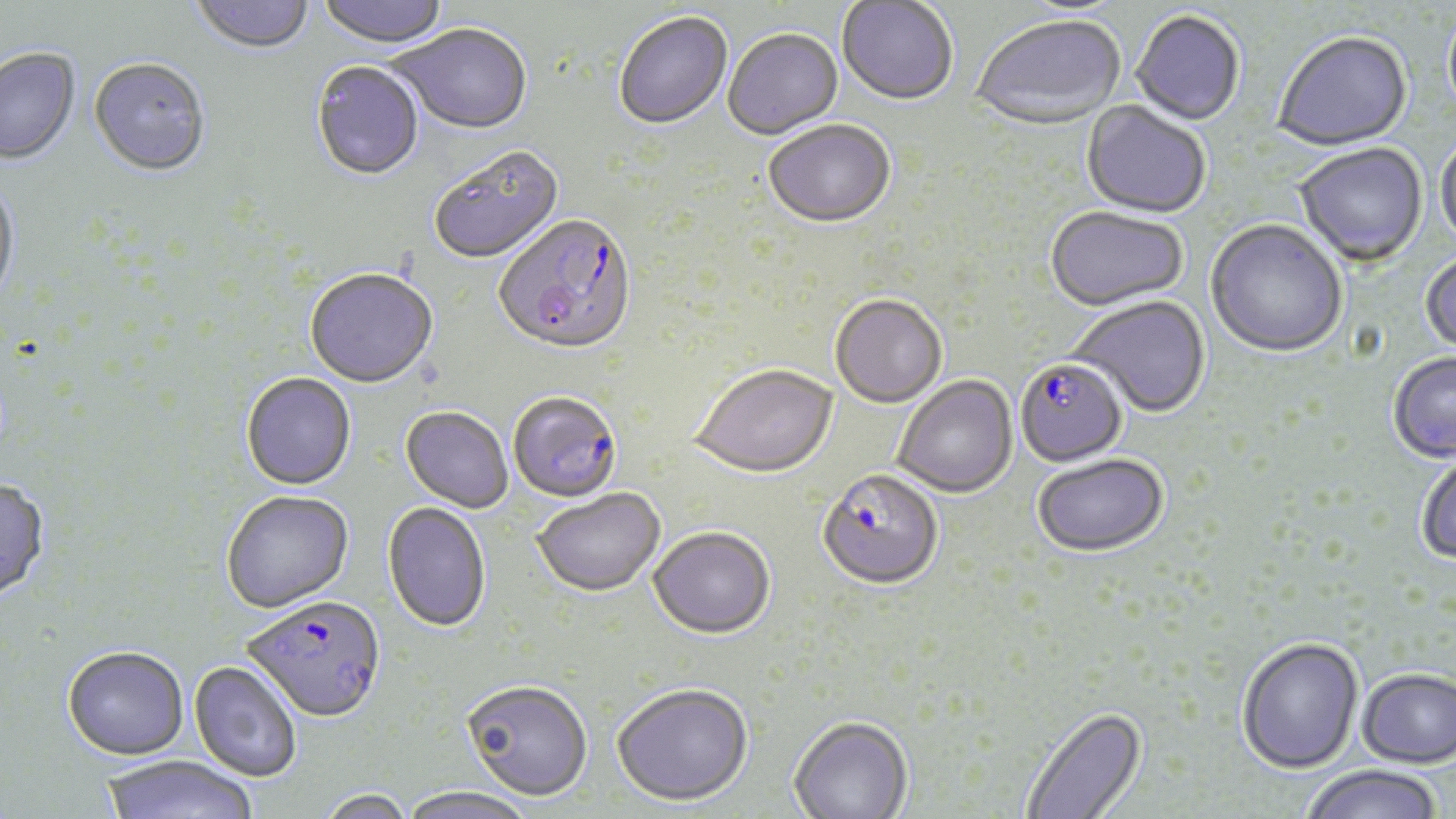

Summary:
  - Coordinate format: approximate bounding boxes as (x1, y1, x2, y2) in pixels
  - Uninfected red blood cell locations: (190, 0, 314, 57), (317, 0, 449, 52), (837, 2, 958, 108), (1443, 4, 1456, 128), (1131, 12, 1245, 127), (614, 13, 732, 132), (972, 17, 1126, 132), (390, 26, 532, 137), (723, 30, 843, 142), (1273, 33, 1412, 153), (0, 50, 81, 167), (88, 60, 211, 179), (310, 62, 425, 183), (1080, 101, 1211, 220), (764, 122, 896, 231), (1435, 137, 1456, 252), (1293, 144, 1429, 269), (429, 148, 565, 266), (0, 178, 20, 310), (1045, 209, 1188, 314), (1205, 221, 1347, 360), (1420, 252, 1456, 358), (304, 271, 437, 391), (830, 296, 947, 410), (1070, 297, 1211, 419), (1388, 353, 1456, 464), (690, 367, 839, 481), (240, 374, 356, 492), (893, 376, 1018, 499), (400, 407, 513, 514), (1415, 451, 1456, 565), (1033, 456, 1169, 559), (0, 479, 51, 604), (532, 490, 666, 599), (221, 492, 355, 615), (382, 502, 491, 635), (648, 530, 775, 641), (1236, 636, 1364, 774), (62, 647, 189, 761), (188, 661, 302, 782), (1357, 667, 1456, 767), (461, 682, 592, 803), (612, 686, 753, 809), (1020, 707, 1148, 818), (788, 718, 913, 819), (100, 755, 257, 819), (1300, 765, 1445, 819), (399, 787, 537, 819), (317, 789, 417, 819)
  - Plasmodium falciparum-infected red blood cell locations: (493, 217, 638, 359), (1015, 360, 1128, 469), (508, 391, 630, 510), (818, 472, 942, 592), (244, 600, 387, 726)
  - Slide-level diagnosis: Plasmodium falciparum
  - Stain: May-Grünwald-Giemsa
  - Field of view: one of a larger specimen
  - Preparation: thin blood smear
  - Magnification: 1000x
  - Modality: light microscopy
  - Image size: 1456×819 pixels